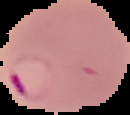
Summary:
  - Malaria status: parasitized
  - Image type: segmented cell region on a black background
  - Preparation: thin blood smear
  - Image size: 130×115 pixels